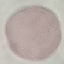
Summary:
  - Malaria status: uninfected
  - Capture: smartphone through the microscope eyepiece
  - Preparation: thin smear
  - Stain: Giemsa
  - Image type: cell patch, automatically extracted from a larger field of view and resized to 64 × 64 pixels